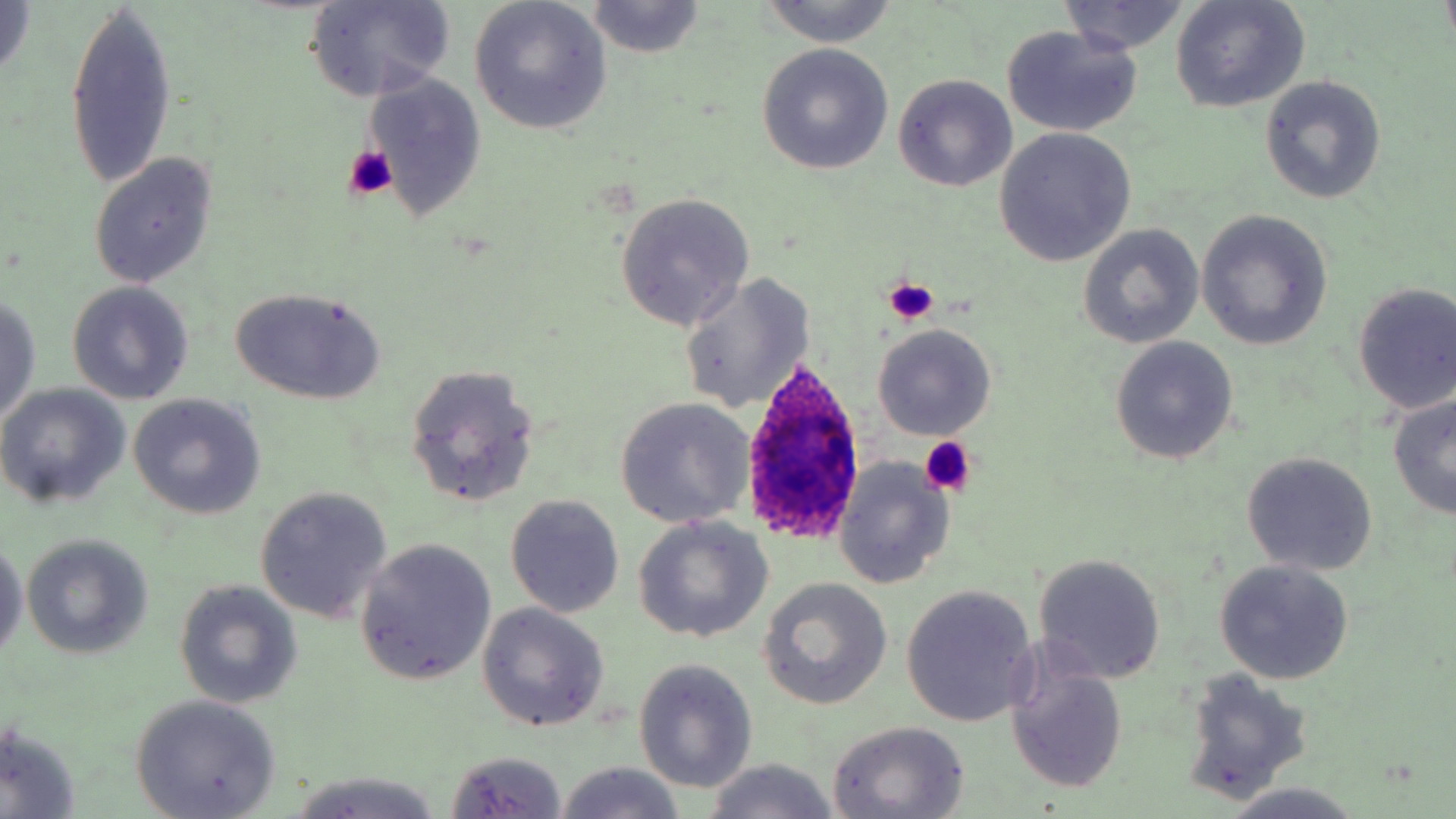

Summary:
  - Coordinate format: approximate bounding boxes as named x1/y1/x2/y2 corners in pixels
  - Platelet locations: (x1=344, y1=147, x2=398, y2=200), (x1=884, y1=278, x2=941, y2=325), (x1=919, y1=437, x2=978, y2=497)
  - Uninfected red blood cell locations: (x1=0, y1=0, x2=36, y2=80), (x1=758, y1=0, x2=901, y2=47), (x1=1057, y1=0, x2=1191, y2=55), (x1=306, y1=1, x2=457, y2=103), (x1=469, y1=1, x2=613, y2=134), (x1=1169, y1=1, x2=1310, y2=112), (x1=64, y1=2, x2=176, y2=193), (x1=586, y1=2, x2=704, y2=57), (x1=1002, y1=26, x2=1142, y2=136), (x1=756, y1=43, x2=895, y2=175), (x1=360, y1=70, x2=488, y2=225), (x1=893, y1=73, x2=1018, y2=191), (x1=1258, y1=78, x2=1387, y2=205), (x1=994, y1=128, x2=1137, y2=268), (x1=88, y1=152, x2=217, y2=289), (x1=614, y1=191, x2=755, y2=331), (x1=1196, y1=210, x2=1333, y2=350), (x1=1078, y1=225, x2=1205, y2=348), (x1=678, y1=272, x2=814, y2=416), (x1=68, y1=282, x2=195, y2=405), (x1=1351, y1=283, x2=1456, y2=415), (x1=229, y1=287, x2=385, y2=405), (x1=0, y1=293, x2=42, y2=425), (x1=872, y1=324, x2=998, y2=440), (x1=1108, y1=336, x2=1238, y2=466), (x1=405, y1=363, x2=540, y2=509), (x1=0, y1=385, x2=131, y2=508), (x1=1386, y1=393, x2=1456, y2=520), (x1=128, y1=394, x2=266, y2=519), (x1=615, y1=397, x2=755, y2=529), (x1=1241, y1=452, x2=1378, y2=576), (x1=834, y1=457, x2=956, y2=589), (x1=255, y1=486, x2=394, y2=625), (x1=505, y1=494, x2=625, y2=617), (x1=633, y1=516, x2=772, y2=643), (x1=22, y1=535, x2=154, y2=660), (x1=0, y1=538, x2=27, y2=661), (x1=355, y1=541, x2=497, y2=684), (x1=1033, y1=554, x2=1166, y2=684), (x1=1213, y1=559, x2=1354, y2=684), (x1=759, y1=579, x2=892, y2=708), (x1=175, y1=581, x2=302, y2=708), (x1=901, y1=585, x2=1039, y2=726), (x1=476, y1=602, x2=610, y2=732), (x1=1004, y1=653, x2=1129, y2=795), (x1=634, y1=658, x2=758, y2=794), (x1=1177, y1=668, x2=1312, y2=805), (x1=130, y1=695, x2=283, y2=818), (x1=826, y1=720, x2=973, y2=818), (x1=0, y1=724, x2=81, y2=819), (x1=446, y1=750, x2=568, y2=818), (x1=699, y1=759, x2=840, y2=819), (x1=554, y1=763, x2=686, y2=818), (x1=287, y1=772, x2=444, y2=819), (x1=1215, y1=785, x2=1367, y2=819)
  - Plasmodium ovale-infected red blood cell locations: (x1=740, y1=354, x2=869, y2=544)
  - Slide-level diagnosis: Plasmodium ovale
  - Preparation: thin blood film
  - Field of view: single
  - Modality: light microscopy
  - Stain: May-Grünwald-Giemsa
  - Image size: 1456×819 pixels
  - Magnification: 1000x